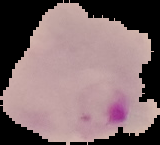

{
  "preparation": "thin blood film",
  "result": "Plasmodium parasites identified",
  "image_type": "segmented cell region on a black background",
  "image_size": "160×145 pixels"
}